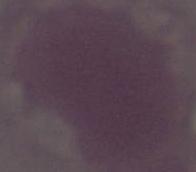
1000x magnification. An erythrocyte is seen. Photomicrograph.